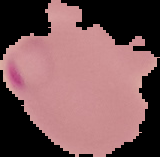 Cell region segmented out of the field of view; the surrounding area is masked to black. Image is 160×157 pixels. From a thin blood smear. Malaria status: parasitized.